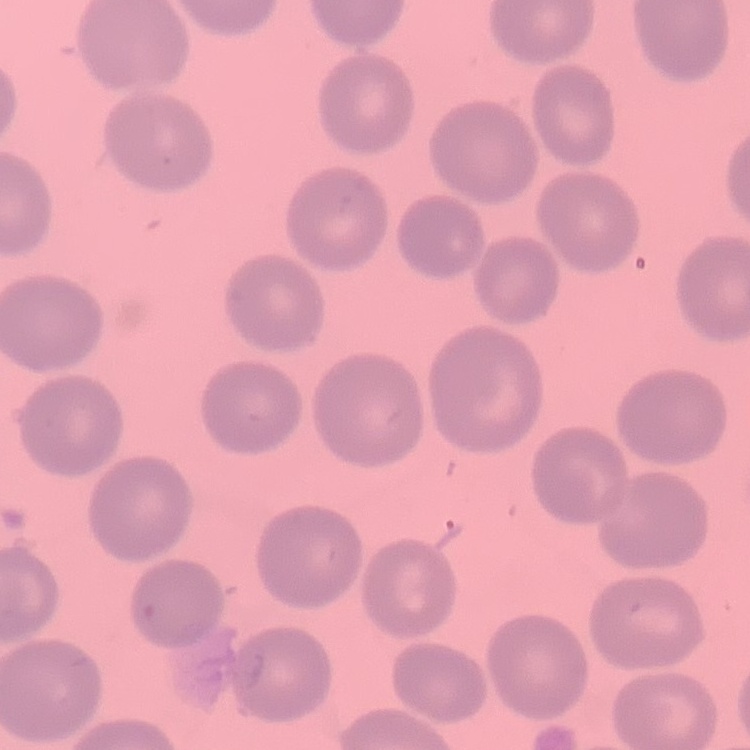
Summary:
  - Erythrocyte morphology: no rouleaux formation
  - Stain: Field's or Giemsa
  - Preparation: thin blood smear
  - Image type: square crop of a larger photomicrograph